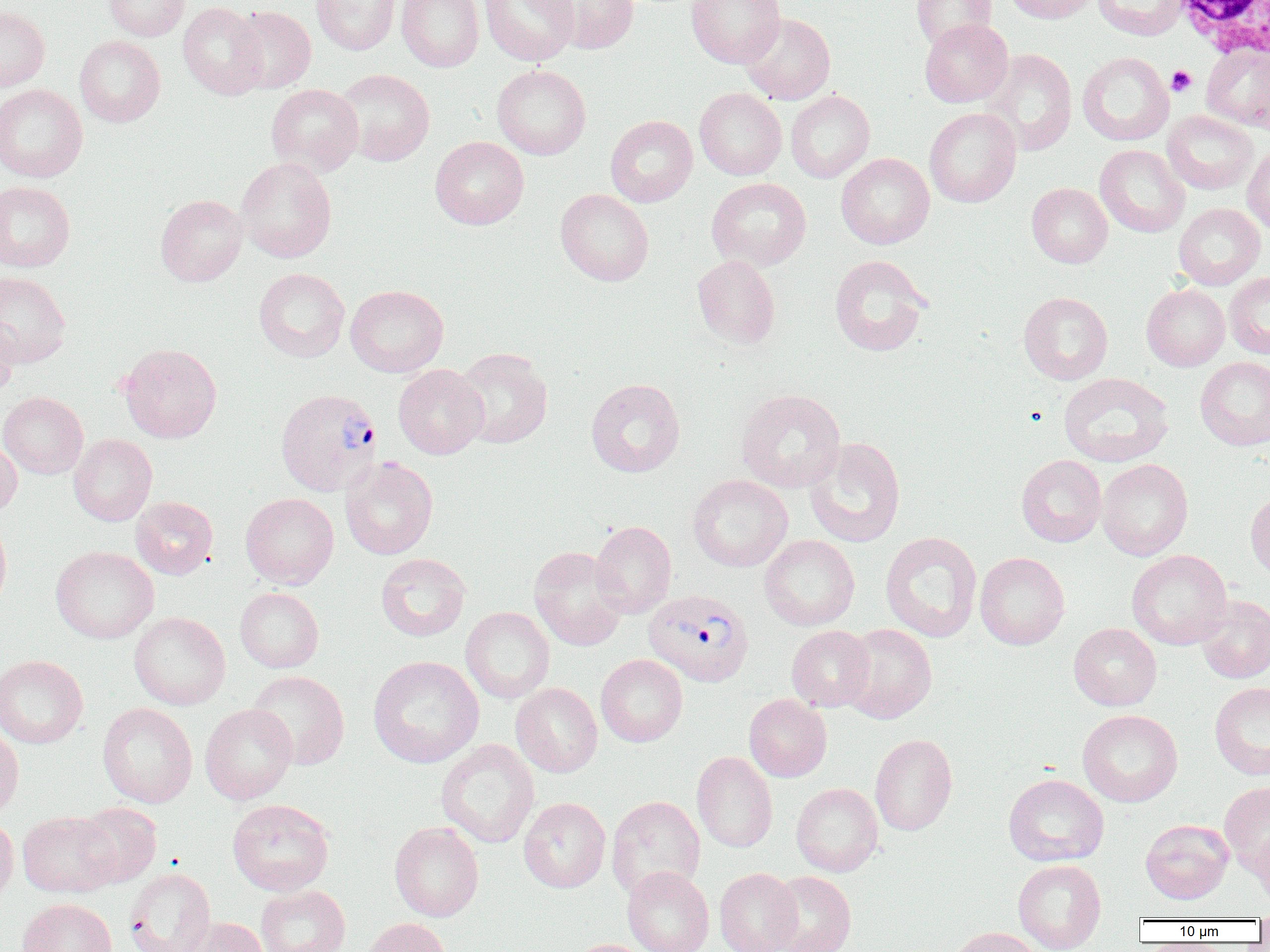

Approximate bounding boxes as named x1/y1/x2/y2 corners in pixels. Plasmodium vivax-infected red blood cell locations: (x1=275, y1=388, x2=382, y2=496), (x1=643, y1=589, x2=754, y2=687). Platelet locations: (x1=1166, y1=65, x2=1196, y2=96). White blood cell locations: (x1=1170, y1=0, x2=1270, y2=59). Uninfected red blood cell locations: (x1=103, y1=0, x2=190, y2=41), (x1=311, y1=0, x2=400, y2=55), (x1=396, y1=0, x2=484, y2=72), (x1=480, y1=0, x2=579, y2=66), (x1=538, y1=0, x2=640, y2=54), (x1=686, y1=0, x2=786, y2=68), (x1=911, y1=0, x2=997, y2=51), (x1=1002, y1=0, x2=1099, y2=24), (x1=1093, y1=0, x2=1189, y2=41), (x1=177, y1=2, x2=267, y2=100), (x1=0, y1=5, x2=50, y2=91), (x1=230, y1=5, x2=316, y2=93), (x1=740, y1=13, x2=835, y2=104), (x1=919, y1=18, x2=1013, y2=107), (x1=74, y1=36, x2=165, y2=127), (x1=1201, y1=44, x2=1270, y2=131), (x1=982, y1=48, x2=1078, y2=156), (x1=1077, y1=52, x2=1174, y2=146), (x1=491, y1=64, x2=591, y2=160), (x1=334, y1=69, x2=435, y2=166), (x1=0, y1=84, x2=88, y2=183), (x1=266, y1=84, x2=363, y2=177), (x1=694, y1=88, x2=787, y2=180), (x1=786, y1=90, x2=875, y2=183), (x1=924, y1=108, x2=1021, y2=208), (x1=1162, y1=111, x2=1259, y2=194), (x1=605, y1=115, x2=697, y2=207), (x1=430, y1=136, x2=529, y2=229), (x1=1095, y1=144, x2=1189, y2=238), (x1=1242, y1=144, x2=1270, y2=236), (x1=836, y1=152, x2=935, y2=249), (x1=235, y1=157, x2=337, y2=263), (x1=706, y1=177, x2=811, y2=271), (x1=0, y1=181, x2=75, y2=272), (x1=1026, y1=183, x2=1113, y2=268), (x1=555, y1=189, x2=654, y2=285), (x1=155, y1=194, x2=247, y2=286), (x1=1173, y1=203, x2=1265, y2=289), (x1=829, y1=254, x2=931, y2=356), (x1=692, y1=255, x2=781, y2=349), (x1=254, y1=268, x2=349, y2=362), (x1=0, y1=271, x2=71, y2=367), (x1=1224, y1=272, x2=1270, y2=359), (x1=1141, y1=283, x2=1230, y2=371), (x1=345, y1=284, x2=448, y2=377), (x1=1018, y1=291, x2=1113, y2=384), (x1=0, y1=314, x2=18, y2=400), (x1=119, y1=343, x2=222, y2=443), (x1=453, y1=347, x2=552, y2=448), (x1=1195, y1=357, x2=1270, y2=450), (x1=393, y1=364, x2=488, y2=459), (x1=1058, y1=373, x2=1174, y2=467), (x1=586, y1=378, x2=685, y2=477), (x1=736, y1=389, x2=846, y2=493), (x1=0, y1=391, x2=88, y2=478), (x1=69, y1=434, x2=157, y2=526), (x1=0, y1=436, x2=22, y2=515), (x1=804, y1=437, x2=906, y2=547), (x1=1016, y1=455, x2=1106, y2=547), (x1=340, y1=457, x2=438, y2=560), (x1=1097, y1=459, x2=1193, y2=561), (x1=688, y1=475, x2=792, y2=572), (x1=1245, y1=491, x2=1270, y2=581), (x1=240, y1=493, x2=339, y2=589), (x1=131, y1=496, x2=218, y2=579), (x1=0, y1=515, x2=12, y2=617), (x1=590, y1=521, x2=676, y2=618), (x1=879, y1=531, x2=982, y2=642), (x1=759, y1=534, x2=860, y2=631), (x1=51, y1=546, x2=159, y2=644), (x1=529, y1=546, x2=628, y2=651), (x1=1126, y1=549, x2=1232, y2=650), (x1=375, y1=552, x2=471, y2=641), (x1=975, y1=552, x2=1070, y2=650), (x1=235, y1=587, x2=324, y2=672), (x1=1195, y1=595, x2=1270, y2=683), (x1=460, y1=607, x2=554, y2=703), (x1=129, y1=611, x2=231, y2=710), (x1=839, y1=623, x2=937, y2=723), (x1=1068, y1=623, x2=1162, y2=711), (x1=787, y1=625, x2=875, y2=712), (x1=0, y1=654, x2=88, y2=748), (x1=596, y1=654, x2=688, y2=747), (x1=368, y1=655, x2=484, y2=768), (x1=248, y1=670, x2=350, y2=770), (x1=1209, y1=681, x2=1270, y2=780), (x1=511, y1=683, x2=602, y2=777), (x1=744, y1=694, x2=832, y2=782), (x1=97, y1=703, x2=197, y2=807), (x1=200, y1=703, x2=297, y2=804), (x1=1077, y1=709, x2=1183, y2=807), (x1=0, y1=723, x2=24, y2=822), (x1=869, y1=733, x2=958, y2=836), (x1=436, y1=739, x2=539, y2=848), (x1=691, y1=752, x2=777, y2=853), (x1=1003, y1=773, x2=1109, y2=866), (x1=1219, y1=781, x2=1270, y2=874), (x1=791, y1=782, x2=883, y2=876), (x1=606, y1=795, x2=705, y2=900), (x1=519, y1=797, x2=611, y2=893), (x1=227, y1=799, x2=335, y2=896), (x1=71, y1=802, x2=161, y2=888), (x1=18, y1=811, x2=119, y2=897), (x1=0, y1=816, x2=18, y2=908), (x1=1140, y1=819, x2=1233, y2=904), (x1=389, y1=821, x2=484, y2=921), (x1=1253, y1=827, x2=1270, y2=910), (x1=1013, y1=859, x2=1106, y2=952), (x1=622, y1=866, x2=714, y2=952), (x1=123, y1=867, x2=215, y2=952), (x1=715, y1=867, x2=802, y2=952), (x1=765, y1=871, x2=857, y2=952), (x1=255, y1=884, x2=350, y2=952), (x1=17, y1=898, x2=118, y2=952), (x1=1254, y1=909, x2=1270, y2=939), (x1=178, y1=917, x2=269, y2=952), (x1=361, y1=918, x2=452, y2=952), (x1=946, y1=926, x2=1046, y2=952), (x1=569, y1=939, x2=656, y2=952). Slide-level diagnosis: Plasmodium vivax. 1000x magnification. Thin blood smear. One field of a larger specimen. Image is 1270×952 pixels. Light microscopy.